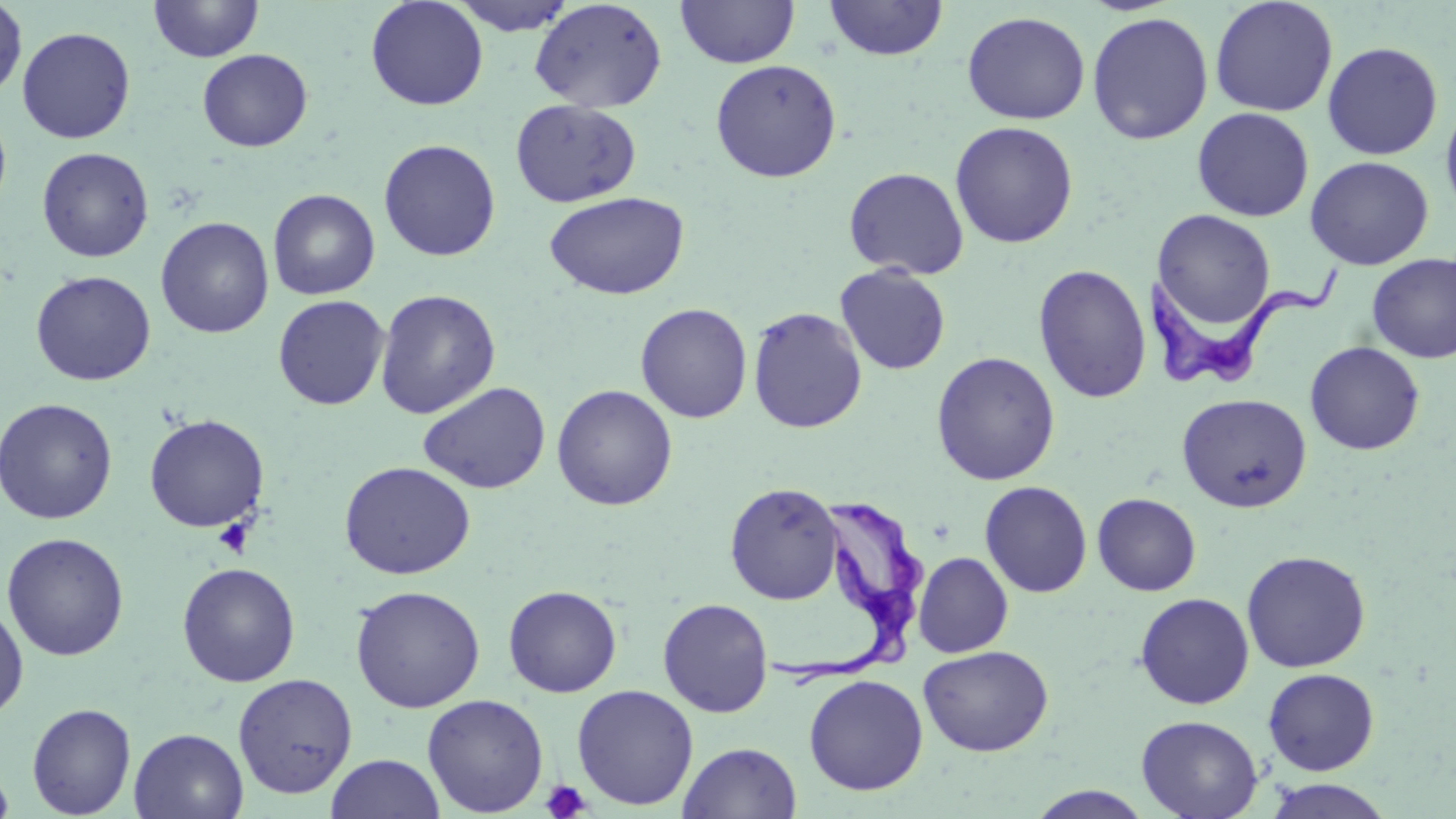
slide-level diagnosis = Trypanosoma brucei
platelet locations = approximate bounding boxes as named x1/y1/x2/y2 corners in pixels: (x1=213, y1=519, x2=253, y2=557), (x1=540, y1=780, x2=591, y2=819)
image size = 1456×819 pixels
Trypanosoma brucei locations = approximate bounding boxes as named x1/y1/x2/y2 corners in pixels: (x1=1140, y1=247, x2=1345, y2=391), (x1=764, y1=479, x2=937, y2=693)
magnification = 1000x
field of view = single
preparation = thin blood film
modality = optical microscopy
stain = May-Grünwald-Giemsa
uninfected red blood cell locations = approximate bounding boxes as named x1/y1/x2/y2 corners in pixels: (x1=365, y1=0, x2=488, y2=111), (x1=449, y1=0, x2=578, y2=36), (x1=675, y1=0, x2=800, y2=69), (x1=824, y1=0, x2=948, y2=61), (x1=1209, y1=0, x2=1338, y2=117), (x1=0, y1=1, x2=27, y2=101), (x1=149, y1=1, x2=263, y2=62), (x1=529, y1=1, x2=667, y2=113), (x1=961, y1=10, x2=1091, y2=124), (x1=1086, y1=11, x2=1214, y2=145), (x1=16, y1=26, x2=136, y2=144), (x1=30, y1=26, x2=144, y2=260), (x1=1322, y1=41, x2=1443, y2=160), (x1=197, y1=49, x2=313, y2=152), (x1=710, y1=59, x2=842, y2=183), (x1=1440, y1=95, x2=1456, y2=224), (x1=510, y1=99, x2=641, y2=208), (x1=0, y1=106, x2=12, y2=218), (x1=1192, y1=107, x2=1314, y2=222), (x1=949, y1=121, x2=1079, y2=249), (x1=378, y1=138, x2=501, y2=261), (x1=37, y1=147, x2=154, y2=263), (x1=1304, y1=156, x2=1434, y2=270), (x1=843, y1=167, x2=969, y2=280), (x1=268, y1=188, x2=380, y2=300), (x1=544, y1=191, x2=690, y2=300), (x1=1152, y1=209, x2=1276, y2=331), (x1=155, y1=216, x2=274, y2=338), (x1=1367, y1=253, x2=1456, y2=363), (x1=835, y1=263, x2=951, y2=375), (x1=1032, y1=264, x2=1152, y2=404), (x1=30, y1=270, x2=156, y2=386), (x1=375, y1=289, x2=501, y2=419), (x1=272, y1=294, x2=390, y2=410), (x1=635, y1=302, x2=753, y2=423), (x1=747, y1=306, x2=868, y2=434), (x1=1304, y1=341, x2=1425, y2=455), (x1=931, y1=351, x2=1061, y2=485), (x1=417, y1=381, x2=551, y2=495), (x1=551, y1=384, x2=678, y2=511), (x1=1176, y1=392, x2=1312, y2=513), (x1=0, y1=398, x2=118, y2=525), (x1=144, y1=414, x2=270, y2=533), (x1=339, y1=461, x2=476, y2=579), (x1=979, y1=480, x2=1092, y2=597), (x1=724, y1=482, x2=845, y2=605), (x1=1092, y1=493, x2=1201, y2=596), (x1=2, y1=532, x2=130, y2=661), (x1=1241, y1=550, x2=1371, y2=672), (x1=913, y1=551, x2=1013, y2=657), (x1=176, y1=562, x2=301, y2=687), (x1=503, y1=584, x2=622, y2=698), (x1=349, y1=585, x2=486, y2=713), (x1=1135, y1=592, x2=1255, y2=709), (x1=657, y1=598, x2=773, y2=717), (x1=0, y1=599, x2=29, y2=722), (x1=918, y1=644, x2=1053, y2=757), (x1=1262, y1=668, x2=1380, y2=776), (x1=232, y1=673, x2=358, y2=799), (x1=804, y1=674, x2=928, y2=795), (x1=571, y1=684, x2=699, y2=811), (x1=422, y1=693, x2=549, y2=817), (x1=27, y1=702, x2=136, y2=818), (x1=1136, y1=714, x2=1263, y2=819), (x1=129, y1=727, x2=249, y2=819), (x1=678, y1=741, x2=802, y2=819), (x1=326, y1=753, x2=444, y2=819), (x1=0, y1=757, x2=14, y2=819), (x1=1262, y1=778, x2=1396, y2=819), (x1=1025, y1=786, x2=1156, y2=818)